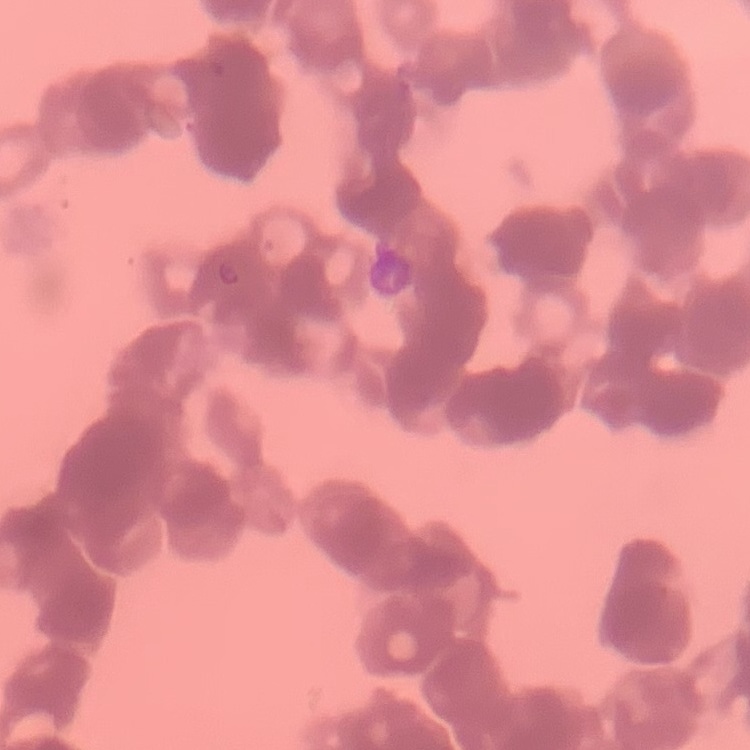

Summary:
  - Red blood cell morphology: rouleaux formation
  - Image type: one tile cut from a larger photomicrograph
  - Stain: Field's or Giemsa
  - Preparation: thin peripheral smear